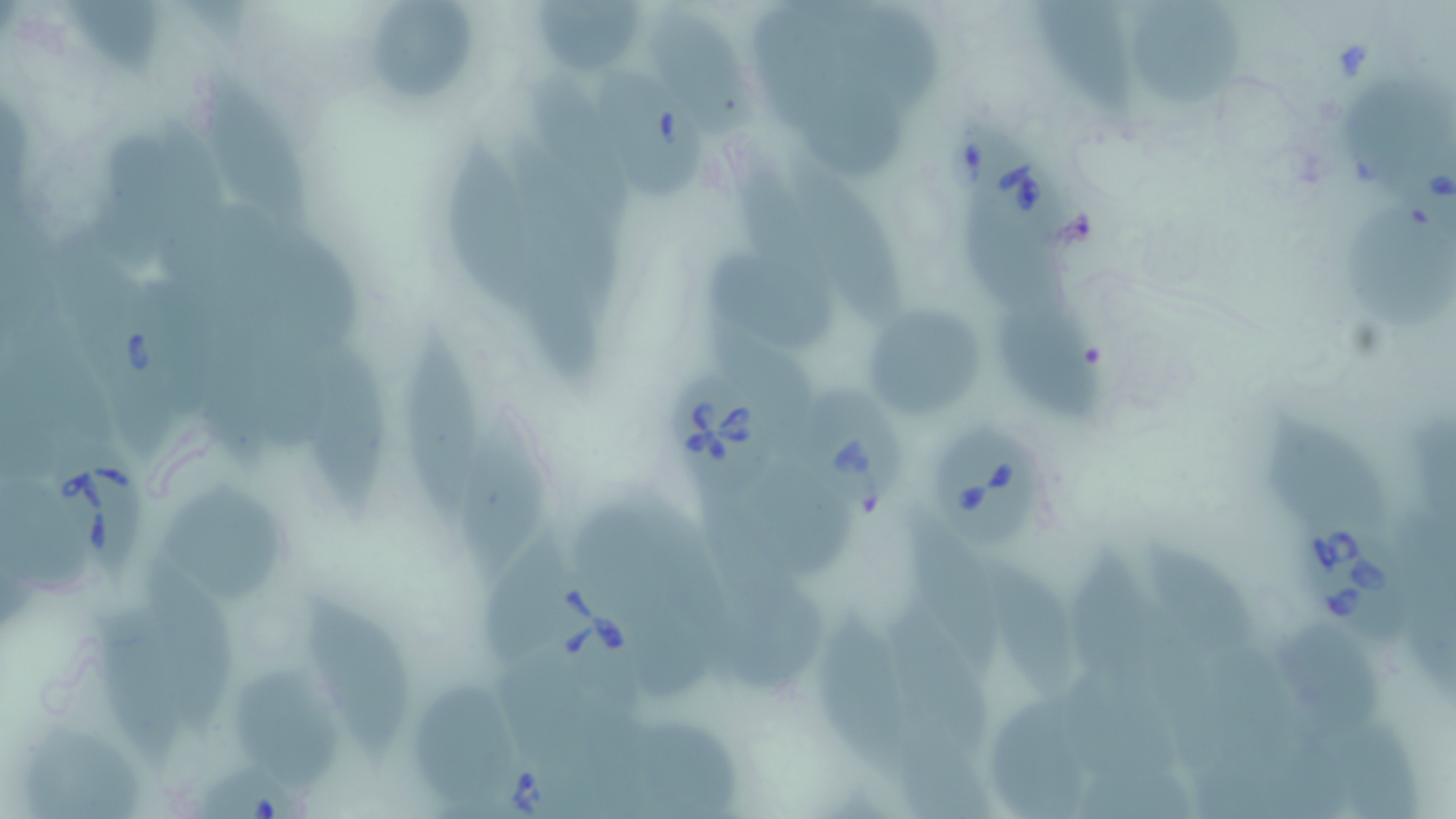

Summary:
  - Coordinate format: approximate bounding boxes as [x1, y1, x2, y2] in pixels
  - Uninfected red blood cell locations: [368, 1, 480, 99], [1030, 1, 1136, 117], [1129, 1, 1248, 110], [535, 3, 649, 68], [1345, 77, 1454, 192], [203, 79, 312, 227], [445, 145, 545, 322], [782, 153, 901, 322], [1343, 202, 1456, 332], [710, 257, 837, 351], [861, 304, 992, 423], [1005, 304, 1110, 419], [394, 333, 484, 515], [306, 346, 390, 520], [454, 406, 550, 582], [1268, 419, 1389, 527], [745, 470, 850, 578], [159, 484, 291, 596], [903, 506, 998, 669], [1140, 540, 1257, 659], [1067, 546, 1156, 692], [985, 563, 1083, 700], [301, 593, 409, 762], [92, 609, 186, 775], [817, 611, 911, 778], [1275, 619, 1385, 741], [231, 666, 347, 785], [416, 686, 512, 812], [991, 700, 1094, 819], [28, 728, 151, 819]
  - Babesia divergens-infected red blood cell locations: [589, 63, 710, 211], [957, 120, 1066, 252], [55, 233, 166, 403], [666, 373, 775, 495], [797, 385, 909, 518], [929, 418, 1050, 559], [45, 429, 146, 581], [1295, 507, 1419, 651], [528, 569, 640, 687], [195, 763, 309, 819]
  - Slide-level diagnosis: Babesia divergens
  - Field of view: single
  - Image size: 1456×819 pixels
  - Preparation: thin blood smear
  - Modality: light microscopy
  - Magnification: 1000x
  - Stain: May-Grünwald-Giemsa